Locate every Plasmodium parasite and every leukocyte.
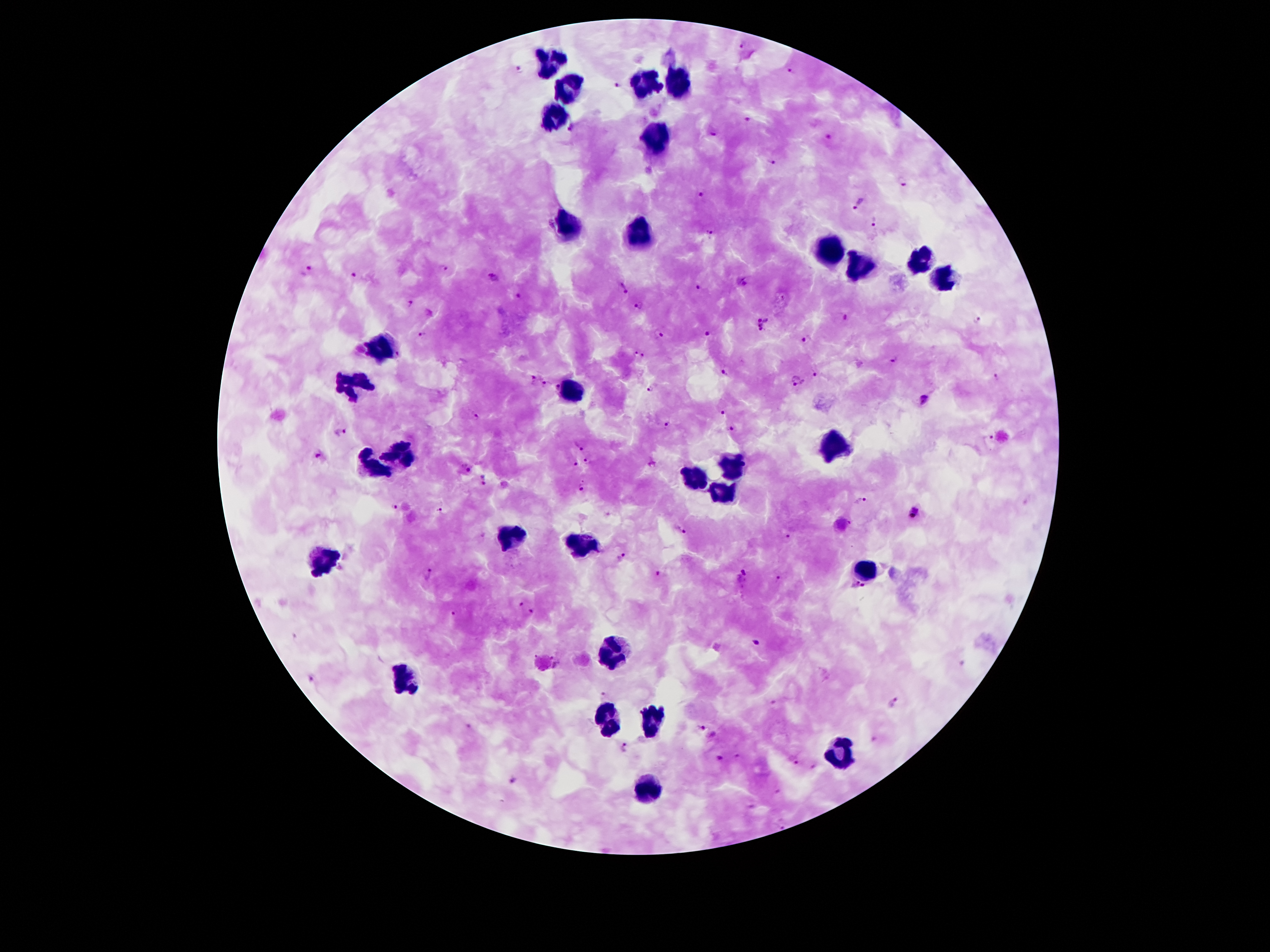

Approximate centers as (x, y) in pixels.
Plasmodium parasites: (744, 45), (519, 68), (792, 71), (617, 84), (747, 119), (572, 126), (712, 132), (828, 135), (771, 163), (901, 183), (702, 193), (858, 203), (875, 221), (710, 233), (443, 266), (306, 271), (354, 274), (493, 279), (741, 280), (624, 288), (698, 288), (518, 297), (411, 302), (640, 304), (845, 319), (977, 321), (763, 324), (708, 332), (660, 334), (421, 335), (806, 337), (638, 354), (892, 359), (724, 372), (817, 375), (997, 377), (533, 379), (796, 380), (546, 383), (557, 386), (651, 386), (924, 398), (723, 413), (476, 415), (666, 421), (732, 429), (341, 431), (988, 439), (578, 447), (316, 457), (589, 461), (575, 463), (651, 463), (466, 467), (484, 480), (584, 485), (861, 501), (394, 507), (440, 509), (912, 512), (682, 530), (785, 538), (623, 556), (659, 572), (429, 574), (742, 576), (777, 580), (858, 586), (521, 603), (531, 611), (455, 612), (755, 642), (961, 662), (311, 676), (605, 696), (772, 703), (892, 703), (468, 726), (701, 726), (874, 741), (624, 747), (718, 758), (791, 760), (812, 767), (513, 780), (776, 791), (752, 806).
Leukocytes: (549, 58), (649, 83), (680, 87), (569, 89), (555, 117), (656, 142), (563, 224), (640, 237), (828, 253), (923, 258), (860, 267), (946, 280), (381, 348), (356, 383), (574, 391), (833, 442), (404, 453), (731, 466), (372, 469), (694, 478), (512, 539), (581, 546), (326, 558), (867, 567), (612, 651), (401, 676), (606, 719), (651, 719), (842, 751), (648, 791).

{
  "magnification": "100x",
  "image_size": "1270×952 pixels",
  "patient_malaria_status": "positive for Plasmodium falciparum",
  "capture": "smartphone camera through the microscope eyepiece",
  "stain": "Giemsa",
  "field_of_view": "single",
  "preparation": "thick peripheral-blood smear"
}